Name the blood parasite species.
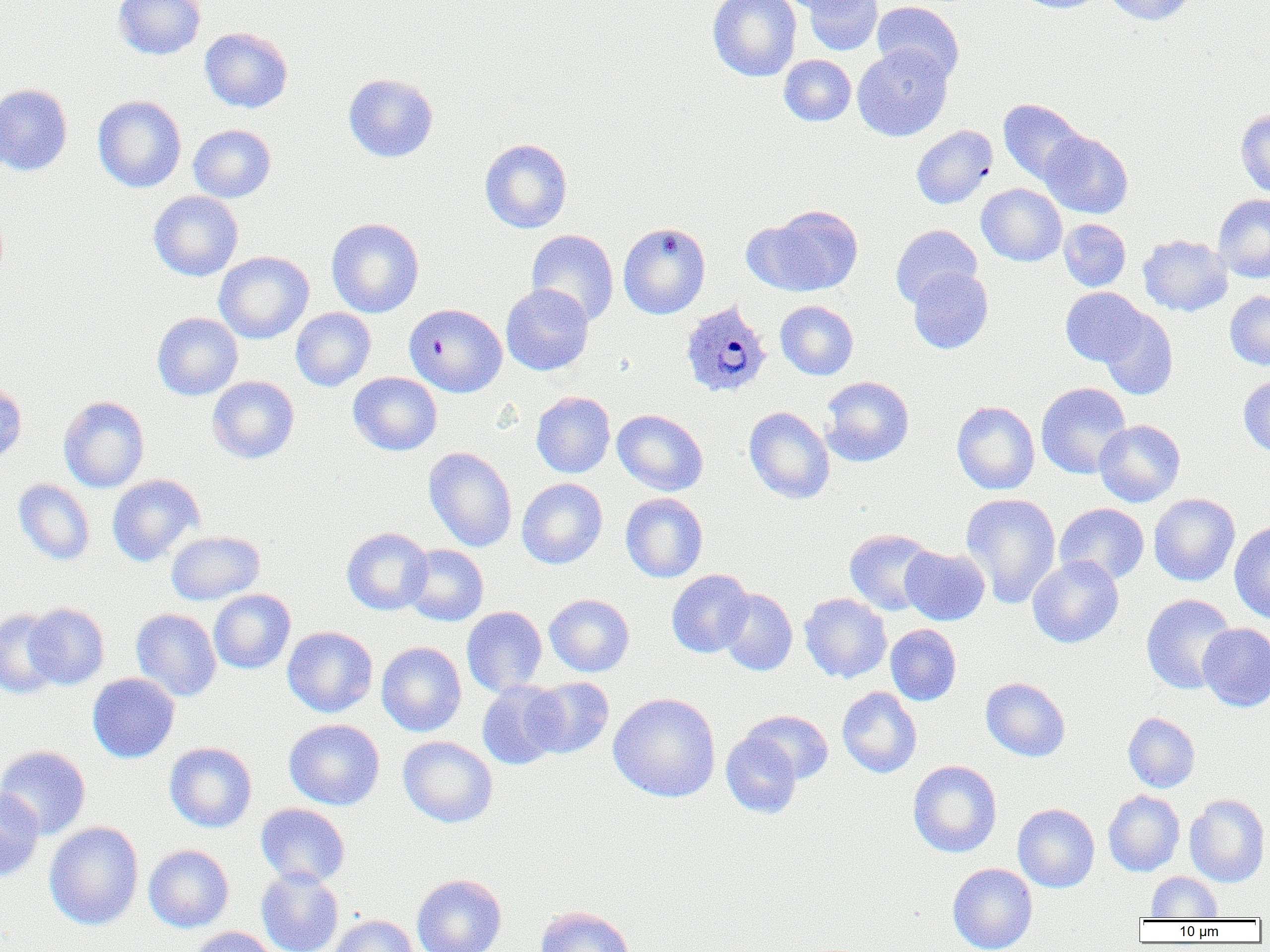
Plasmodium ovale.

Approximate bounding boxes as (x1, y1, x2, y2) in pixels. Plasmodium ovale-infected red blood cell locations: (680, 301, 771, 397). Uninfected red blood cell locations: (113, 0, 206, 60), (708, 0, 801, 81), (777, 0, 866, 15), (804, 0, 883, 55), (1013, 0, 1107, 13), (1105, 0, 1196, 25), (872, 1, 965, 83), (200, 27, 293, 113), (852, 44, 952, 141), (779, 55, 856, 125), (343, 73, 438, 162), (0, 84, 73, 176), (93, 95, 186, 192), (999, 99, 1089, 185), (1236, 109, 1270, 197), (188, 124, 276, 202), (911, 126, 997, 209), (1040, 131, 1133, 219), (480, 139, 572, 233), (977, 184, 1066, 266), (149, 191, 243, 281), (1213, 194, 1270, 282), (754, 205, 863, 296), (326, 218, 424, 317), (1059, 218, 1131, 291), (618, 222, 710, 319), (891, 224, 982, 307), (526, 230, 619, 326), (1138, 235, 1232, 316), (214, 251, 314, 343), (908, 267, 993, 354), (501, 283, 594, 375), (1060, 287, 1149, 366), (1225, 291, 1270, 369), (775, 300, 858, 380), (404, 303, 507, 396), (290, 308, 376, 391), (1097, 308, 1178, 400), (152, 312, 243, 400), (348, 372, 442, 455), (1238, 375, 1270, 456), (207, 376, 299, 464), (819, 376, 914, 466), (0, 381, 27, 464), (1036, 383, 1131, 479), (532, 391, 615, 478), (58, 396, 150, 492), (952, 401, 1039, 494), (744, 406, 834, 505), (612, 409, 708, 495), (1094, 420, 1185, 507), (424, 447, 517, 552), (107, 474, 203, 566), (517, 478, 607, 569), (13, 479, 95, 565), (621, 493, 708, 582), (961, 493, 1061, 608), (1149, 493, 1240, 586), (1054, 503, 1149, 585), (1229, 521, 1270, 624), (342, 527, 432, 615), (844, 528, 937, 616), (166, 531, 265, 605), (403, 544, 488, 626), (900, 545, 990, 625), (1027, 555, 1124, 648), (666, 569, 754, 657), (717, 588, 797, 676), (209, 589, 296, 674), (799, 593, 892, 683), (544, 594, 634, 676), (1141, 594, 1237, 694), (25, 603, 109, 689), (461, 606, 547, 697), (0, 609, 63, 698), (131, 609, 221, 701), (1198, 623, 1270, 711), (885, 624, 962, 705), (282, 626, 377, 717), (377, 642, 467, 736), (87, 673, 179, 763), (523, 677, 615, 759), (981, 677, 1071, 761), (477, 681, 564, 770), (837, 686, 922, 778), (608, 692, 721, 802), (743, 710, 833, 784), (1123, 713, 1200, 792), (284, 719, 384, 810), (721, 730, 803, 819), (398, 736, 498, 828), (164, 742, 257, 833), (0, 745, 91, 839), (908, 760, 1002, 857), (0, 787, 44, 882), (1103, 790, 1184, 876), (1185, 794, 1270, 887), (256, 803, 350, 887), (1013, 804, 1100, 893), (44, 822, 143, 930), (144, 845, 234, 932), (948, 863, 1038, 952), (256, 868, 344, 952), (1146, 872, 1222, 920), (411, 874, 506, 952), (535, 906, 634, 952), (327, 914, 420, 952), (189, 926, 281, 952). Image is 1270×952 pixels. One field of a larger specimen. Captured at 1000x magnification. Thin blood film. Optical microscopy.